Describe the morphology of the red blood cells.
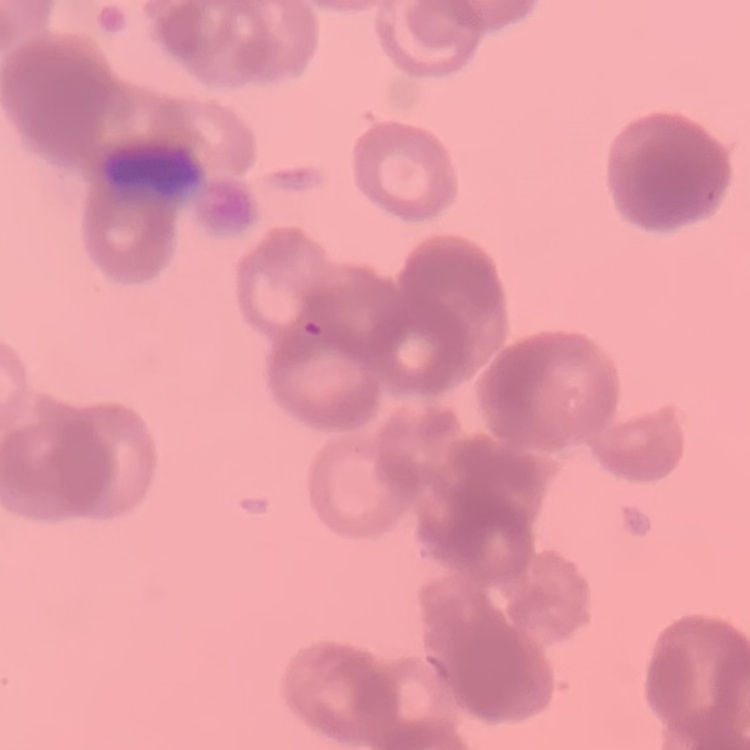

They show rouleaux formation.

Thin blood film. Square crop of a larger photomicrograph. Field's or Giemsa stain.